Point out each Plasmodium parasite.
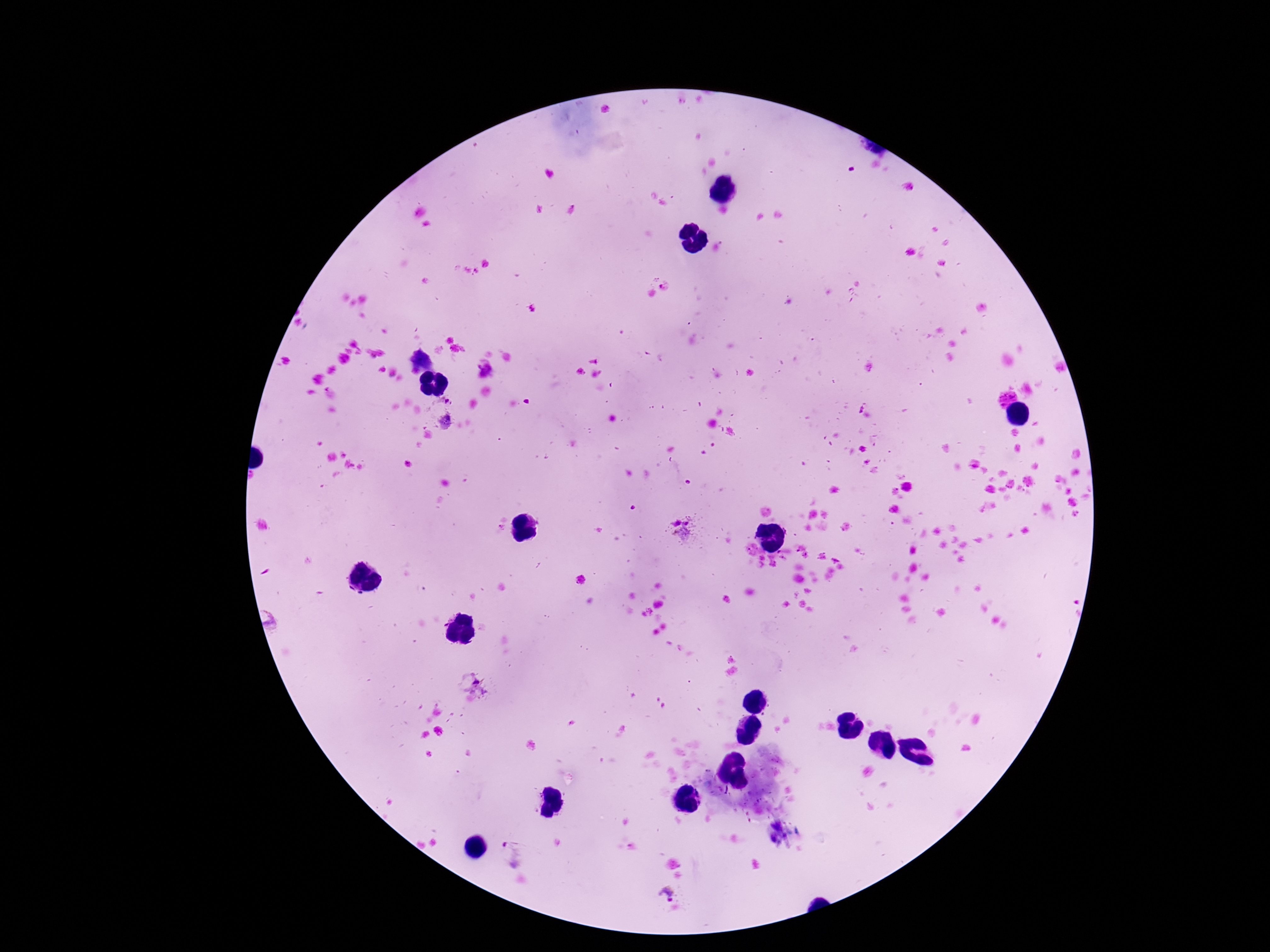

Approximate centers as {x, y} in pixels.
Plasmodium parasites: {486, 369}, {1007, 400}, {443, 413}, {685, 530}, {473, 684}, {514, 854}, {667, 895}.

Giemsa stain. Single field of view. Thick peripheral-blood smear. Photographed through the microscope eyepiece with a smartphone camera. Image is 1270×952 pixels. Patient malaria status: positive. 100x magnification.